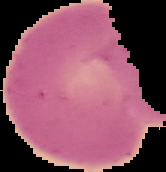

{
  "preparation": "thin blood smear",
  "image_size": "166×172 pixels",
  "result": "no Plasmodium parasites seen",
  "image_type": "cell region segmented out of the field of view; surrounding area masked to black"
}